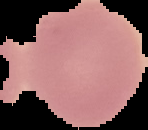

Segmented cell region on a black background. Image is 148×130 pixels. Result: negative for malaria parasites. From a thin blood film.